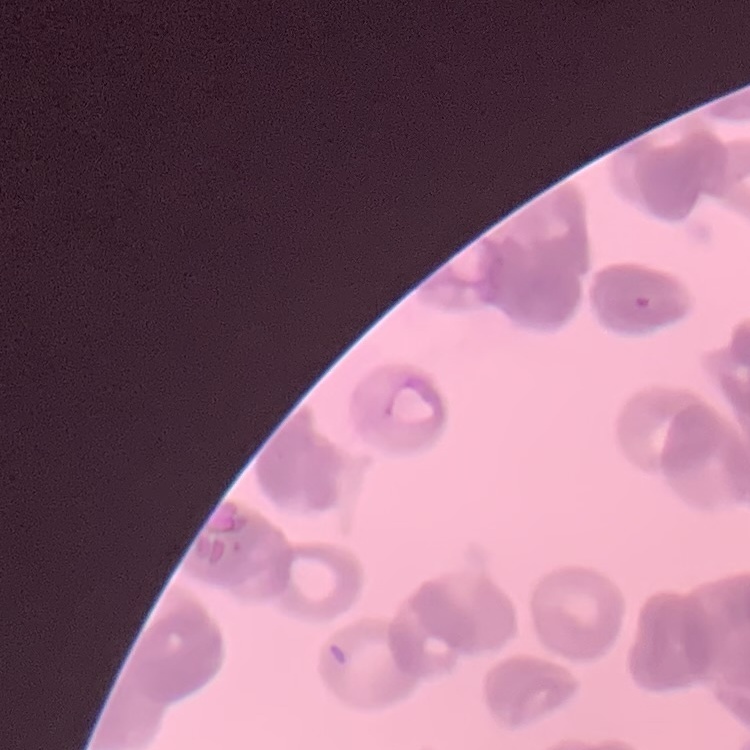

The erythrocytes exhibit rouleaux formation. Field's or Giemsa stain. One tile cut from a larger photomicrograph. Thin blood film.